Classify this cell by malaria status.
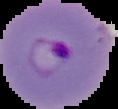

Parasitized.

image size = 118×109 pixels
image type = segmented cell region on a black background
preparation = thin blood film